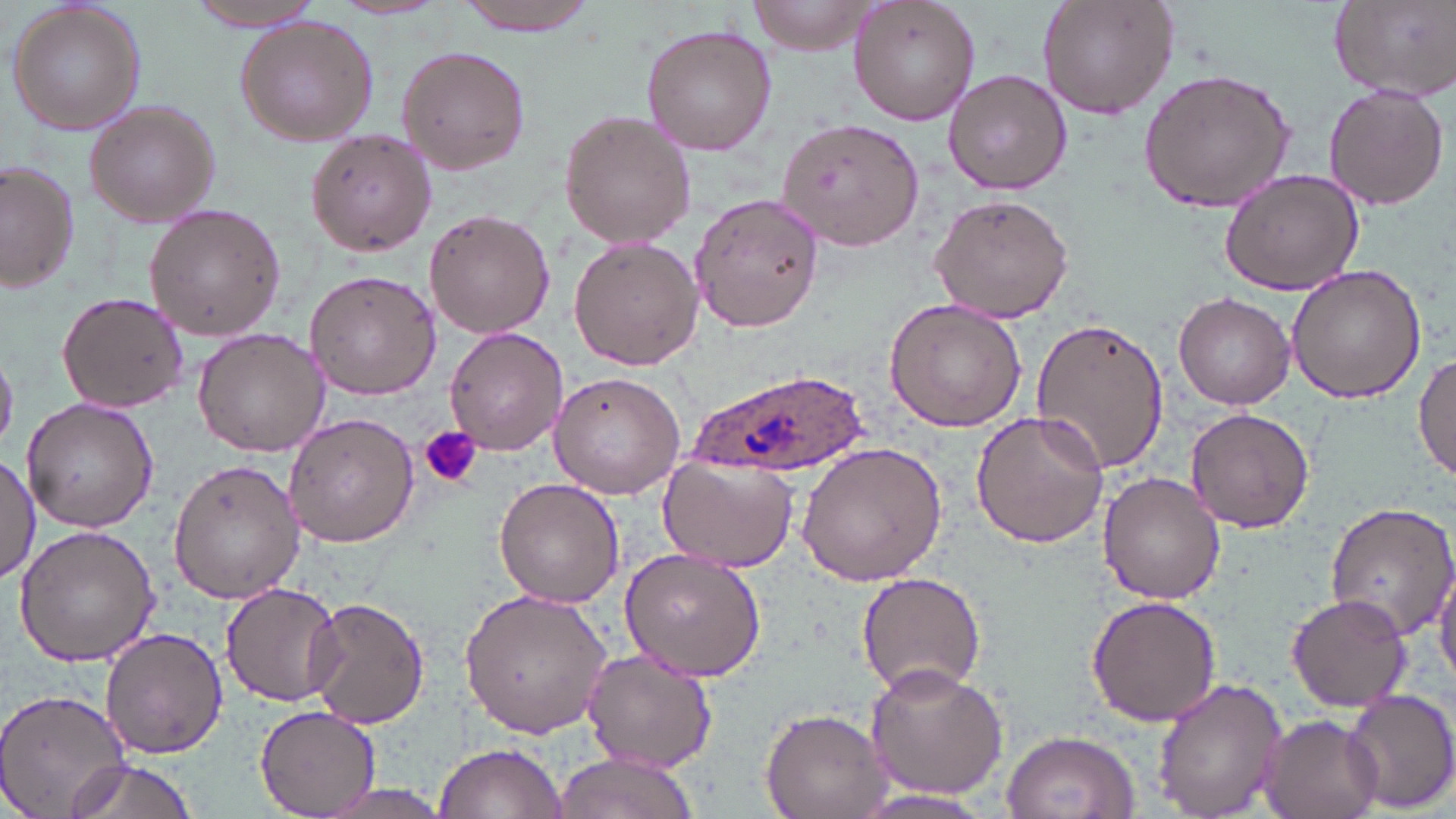

slide-level diagnosis = Plasmodium ovale
magnification = 1000x
uninfected red blood cell locations = approximate bounding boxes as (x1,y1)-(x2,y2) corner pairs in pixels: (187,0)-(328,31), (750,0)-(876,54), (847,0)-(982,126), (1034,0)-(1179,122), (1330,0)-(1456,99), (6,1)-(148,139), (450,1)-(605,35), (234,17)-(377,145), (640,22)-(777,158), (394,44)-(530,175), (943,69)-(1072,195), (1137,69)-(1298,215), (1323,86)-(1450,208), (84,99)-(223,224), (559,109)-(697,250), (776,115)-(927,252), (306,128)-(438,257), (0,161)-(77,295), (1219,167)-(1364,296), (688,192)-(825,332), (926,192)-(1075,324), (143,205)-(284,342), (424,209)-(555,339), (569,236)-(703,371), (1285,261)-(1428,403), (304,270)-(442,399), (56,291)-(189,414), (1174,291)-(1295,409), (885,297)-(1027,432), (1029,317)-(1168,475), (443,325)-(568,456), (192,328)-(332,459), (1414,352)-(1456,482), (546,371)-(687,500), (24,397)-(157,534), (1183,406)-(1315,534), (971,409)-(1109,549), (283,412)-(418,548), (794,440)-(948,587), (1,453)-(38,588), (657,455)-(798,571), (168,458)-(303,604), (1099,472)-(1225,604), (493,477)-(625,609), (1323,500)-(1456,643), (13,525)-(160,666), (619,550)-(768,683), (1431,553)-(1456,686), (856,574)-(986,697), (222,580)-(341,708), (459,588)-(614,738), (1086,593)-(1222,724), (1286,593)-(1410,712), (303,598)-(430,729), (99,626)-(228,760), (581,649)-(716,773), (863,661)-(1010,802), (1153,679)-(1288,816), (1337,687)-(1456,814), (1,688)-(133,819), (256,703)-(380,816), (760,707)-(891,818), (1257,714)-(1383,819), (1001,729)-(1138,818), (434,741)-(567,819), (552,752)-(701,819), (62,757)-(200,819), (848,790)-(1001,818)
image size = 1456×819 pixels
modality = optical microscopy
preparation = thin blood smear
stain = May-Grünwald-Giemsa
Plasmodium ovale-infected red blood cell locations = approximate bounding boxes as (x1,y1)-(x2,y2) corner pairs in pixels: (694,363)-(865,474)
field of view = single
platelet locations = approximate bounding boxes as (x1,y1)-(x2,y2) corner pairs in pixels: (421,426)-(481,490)